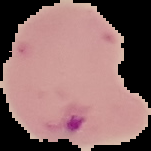
preparation: thin blood smear
result: Plasmodium parasites detected
image_type: segmented cell region on a black background
image_size: 151×151 pixels